Assess this cell for malaria.
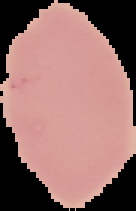
Uninfected.

image type = segmented cell region with the area outside set to black
image size = 136×211 pixels
preparation = thin blood smear